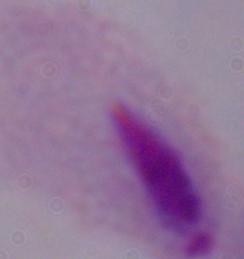
Summary:
  - Magnification: 1000x
  - Identification: trichomonad
  - Modality: photomicrograph